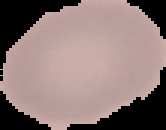
{
  "image_type": "segmented cell region on a black background",
  "preparation": "thin blood smear",
  "malaria_status": "uninfected",
  "image_size": "166×130 pixels"
}